State which parasite is depicted.
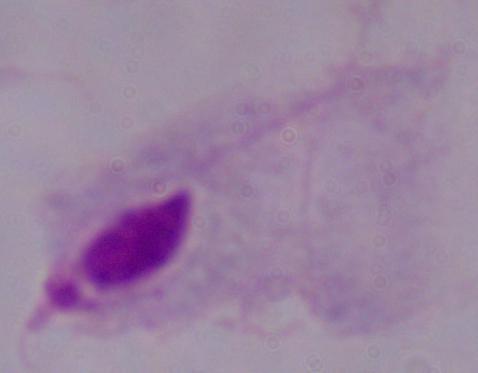

A trichomonad.

Summary:
  - Magnification: 1000x
  - Modality: micrograph